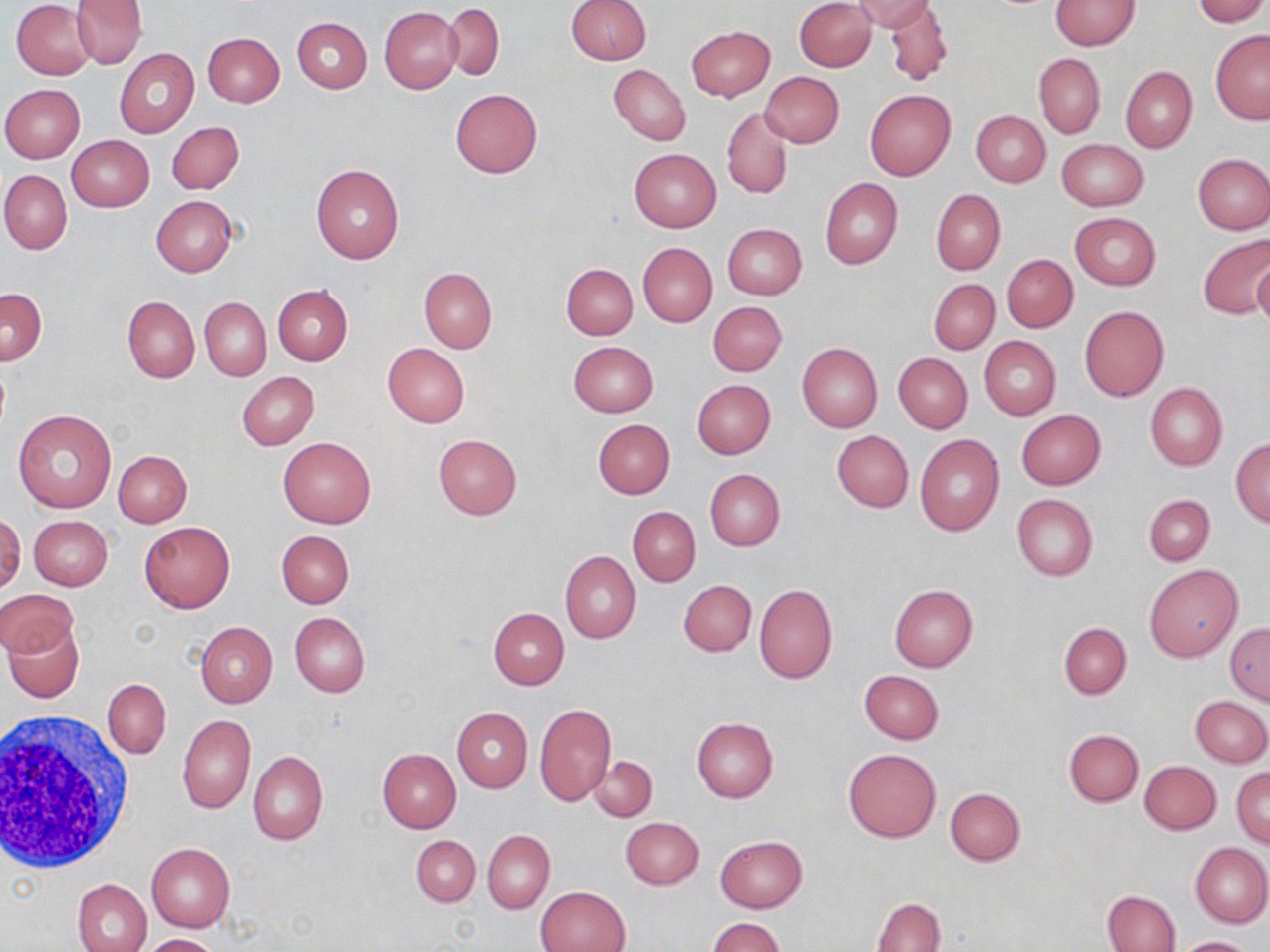 Approximate bounding boxes as (x1, y1, x2, y2) in pixels. Uninfected red blood cell locations: (71, 0, 146, 69), (565, 0, 651, 64), (795, 0, 875, 72), (854, 0, 936, 33), (1192, 0, 1267, 26), (1049, 1, 1139, 50), (12, 2, 98, 80), (884, 2, 953, 87), (442, 4, 504, 80), (379, 6, 462, 94), (291, 17, 371, 93), (687, 25, 774, 101), (1210, 29, 1270, 124), (202, 32, 285, 107), (115, 48, 199, 138), (1034, 52, 1105, 139), (609, 65, 691, 146), (1120, 66, 1197, 152), (759, 71, 844, 147), (1, 85, 85, 162), (450, 88, 542, 178), (864, 89, 955, 181), (722, 109, 793, 199), (971, 110, 1050, 187), (167, 122, 244, 194), (67, 134, 155, 212), (1055, 138, 1148, 211), (629, 148, 722, 232), (1193, 154, 1270, 233), (310, 163, 405, 264), (1, 171, 72, 255), (820, 178, 901, 270), (930, 189, 1005, 275), (152, 196, 236, 276), (1070, 212, 1161, 290), (722, 223, 807, 300), (1199, 233, 1270, 319), (638, 243, 716, 326), (1002, 254, 1078, 332), (1252, 258, 1270, 332), (561, 264, 637, 340), (418, 268, 496, 353), (929, 279, 998, 354), (273, 284, 352, 365), (0, 288, 48, 364), (123, 295, 199, 382), (201, 297, 271, 380), (707, 301, 786, 376), (1079, 305, 1168, 401), (979, 335, 1060, 419), (568, 341, 658, 416), (382, 343, 469, 428), (797, 343, 882, 432), (893, 353, 972, 433), (237, 371, 318, 449), (692, 379, 775, 459), (1145, 383, 1228, 470), (13, 409, 117, 513), (1016, 409, 1105, 490), (593, 419, 675, 499), (831, 430, 914, 512), (433, 433, 522, 519), (914, 433, 1004, 536), (277, 435, 376, 528), (1230, 437, 1270, 526), (114, 450, 192, 527), (705, 469, 785, 550), (1143, 494, 1214, 566), (1012, 495, 1098, 580), (628, 506, 700, 586), (0, 514, 25, 595), (28, 515, 113, 590), (139, 522, 234, 612), (276, 530, 353, 608), (559, 551, 640, 643), (1145, 564, 1242, 662), (678, 579, 757, 657), (754, 584, 838, 685), (889, 585, 977, 672), (0, 588, 78, 658), (489, 607, 569, 690), (290, 612, 369, 697), (195, 622, 279, 707), (1059, 622, 1131, 699), (5, 623, 84, 703), (1226, 623, 1270, 704), (859, 671, 943, 744), (103, 678, 171, 758), (1189, 696, 1269, 768), (534, 704, 617, 807), (452, 708, 532, 792), (178, 714, 255, 814), (691, 717, 778, 801), (1063, 728, 1143, 806), (377, 748, 461, 831), (843, 748, 940, 843), (248, 750, 328, 845), (589, 757, 657, 821), (1139, 760, 1220, 833), (1232, 767, 1270, 848), (945, 787, 1025, 865), (621, 817, 704, 889), (482, 830, 555, 913), (411, 835, 479, 907), (715, 835, 806, 913), (146, 842, 235, 931), (1190, 842, 1270, 927), (73, 878, 152, 952), (536, 885, 630, 952), (1101, 890, 1179, 952), (872, 897, 945, 951), (708, 917, 784, 952), (141, 934, 221, 952), (1175, 936, 1255, 952). White blood cell locations: (1, 711, 139, 873). Slide-level diagnosis: negative for blood parasites. Single field of view. Captured at 1000x magnification. Optical microscopy. Image is 1270×952 pixels. May-Grünwald-Giemsa-stained preparation. Thin blood film.